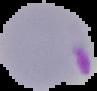
Summary:
  - Image type: cell region segmented out of the field of view; surrounding area masked to black
  - Image size: 97×91 pixels
  - Malaria status: parasitized
  - Preparation: thin blood smear